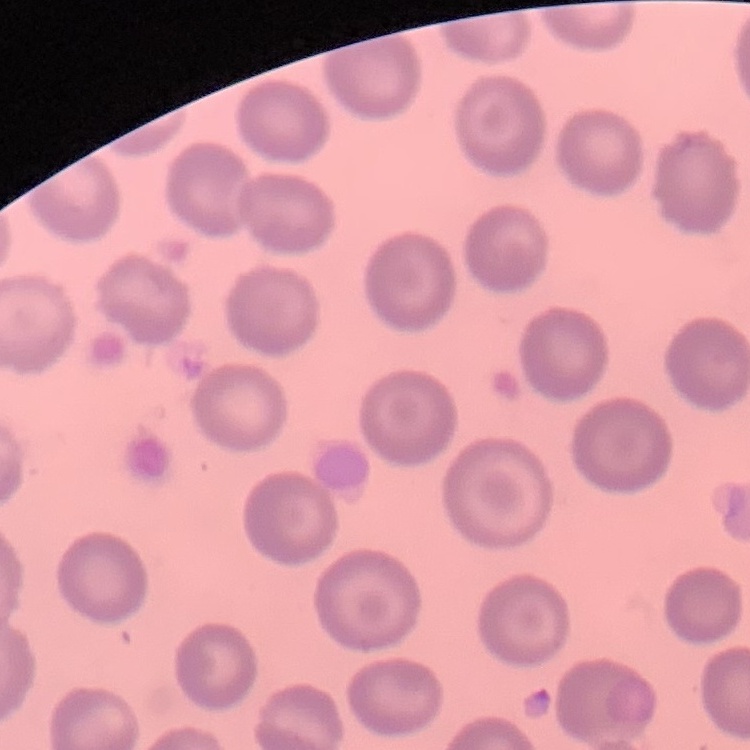

The red blood cells show no rouleaux formation. Thin blood smear. One tile cut from a larger photomicrograph. Stained with either Field's or Giemsa.